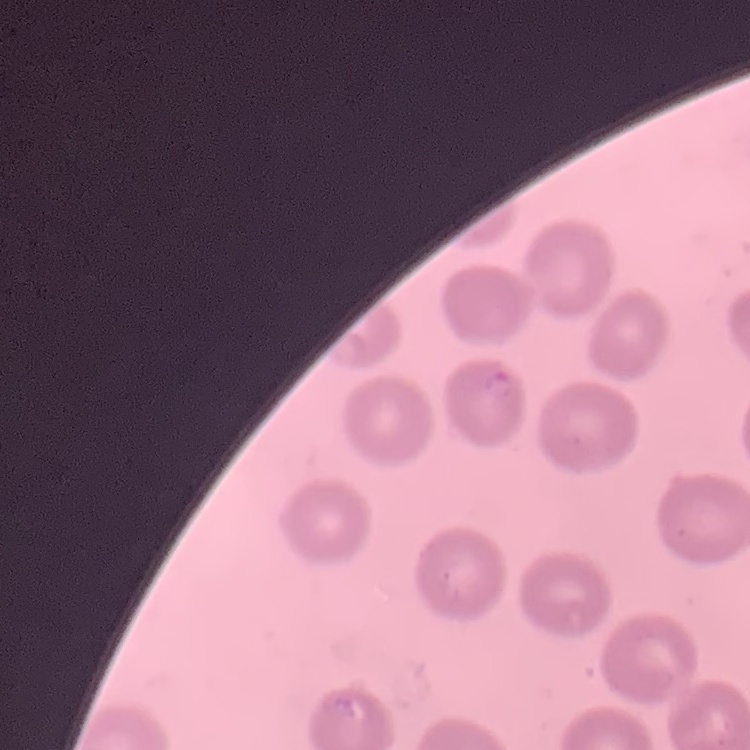
{
  "erythrocyte_morphology": "no rouleaux formation",
  "stain": "Field's or Giemsa",
  "image_type": "one tile cut from a larger photomicrograph",
  "preparation": "thin peripheral smear"
}